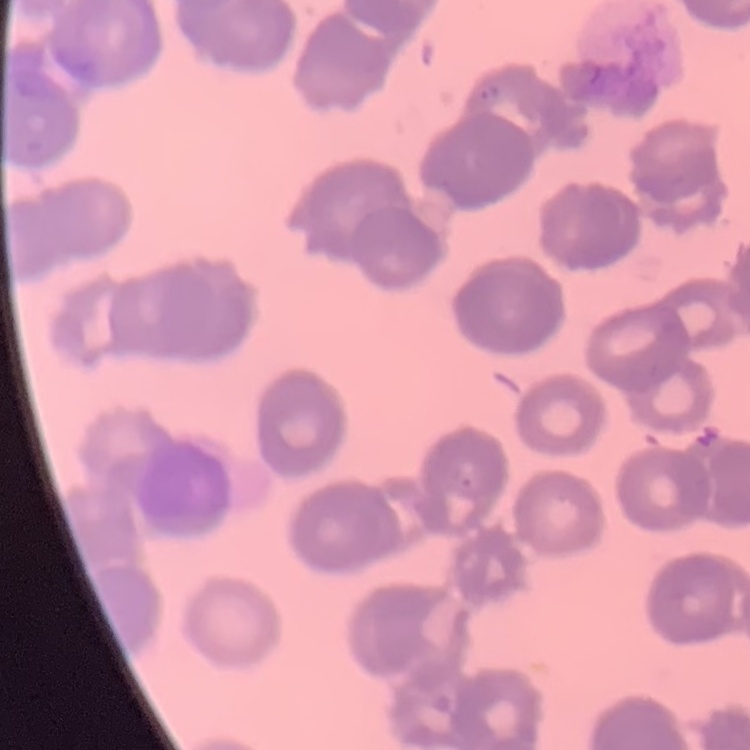
The red blood cells show rouleaux formation. Stained with either Field's or Giemsa. One tile cut from a larger photomicrograph. Thin blood film.